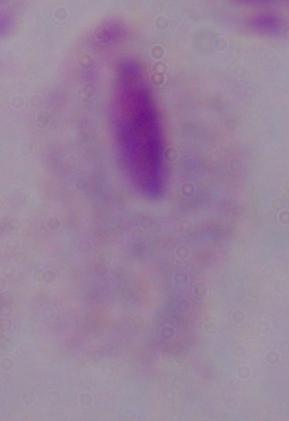
modality = micrograph
magnification = 1000x
identification = trichomonad